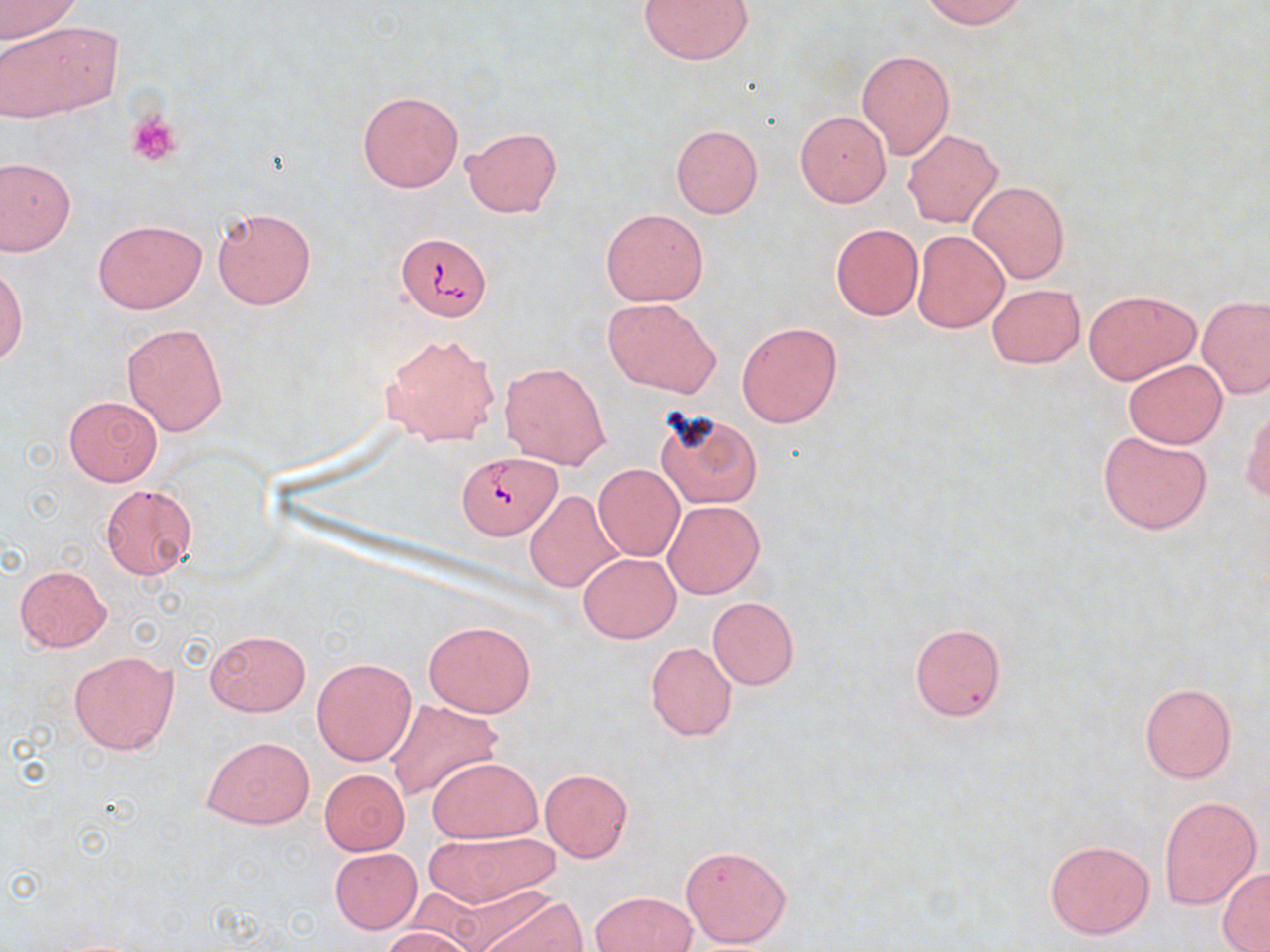
{
  "slide_level_diagnosis": "Babesia divergens",
  "stain": "May-Grünwald-Giemsa",
  "modality": "light microscopy",
  "platelet_locations": "approximate bounding boxes as [x1, y1, x2, y2] in pixels: [127, 109, 185, 169]",
  "field_of_view": "single",
  "uninfected_red_blood_cell_locations": "approximate bounding boxes as [x1, y1, x2, y2] in pixels: [1, 0, 82, 43], [638, 0, 754, 65], [921, 0, 1027, 29], [0, 18, 122, 122], [856, 49, 955, 159], [357, 90, 463, 193], [795, 111, 891, 206], [670, 124, 763, 218], [461, 125, 563, 218], [903, 130, 1002, 227], [2, 157, 74, 254], [967, 179, 1070, 285], [212, 207, 316, 310], [601, 208, 708, 306], [92, 218, 206, 313], [830, 223, 922, 320], [912, 230, 1009, 333], [0, 261, 28, 366], [986, 283, 1085, 368], [1082, 289, 1200, 385], [602, 297, 722, 398], [1196, 297, 1270, 398], [736, 321, 842, 428], [121, 322, 229, 437], [380, 332, 501, 446], [1122, 359, 1228, 448], [499, 360, 611, 469], [63, 396, 162, 487], [1242, 404, 1270, 503], [653, 408, 764, 512], [1097, 428, 1211, 535], [593, 463, 684, 560], [99, 484, 198, 581], [524, 490, 625, 592], [663, 500, 765, 599], [578, 552, 681, 643], [14, 564, 111, 652], [707, 596, 798, 689], [424, 619, 536, 717], [908, 622, 1006, 721], [205, 627, 311, 717], [644, 640, 738, 742], [69, 650, 179, 755], [313, 657, 417, 766], [1139, 681, 1236, 782], [386, 698, 503, 802], [202, 736, 314, 829], [426, 756, 542, 842], [319, 768, 409, 855], [539, 768, 632, 863], [1159, 796, 1261, 910], [430, 830, 557, 907], [1044, 838, 1154, 938], [678, 844, 792, 948], [331, 848, 422, 933], [1218, 868, 1270, 951], [465, 888, 584, 952], [590, 890, 697, 952], [381, 926, 476, 952]",
  "magnification": "1000x",
  "preparation": "thin blood smear",
  "babesia_divergens_infected_red_blood_cell_locations": "approximate bounding boxes as [x1, y1, x2, y2] in pixels: [395, 232, 491, 322], [457, 453, 560, 540]",
  "image_size": "1270×952 pixels"
}